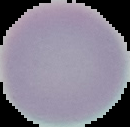

{
  "image_size": "130×127 pixels",
  "image_type": "segmented cell region on a black background",
  "result": "negative for malaria parasites",
  "preparation": "thin blood film"
}